Report the malaria status of this cell.
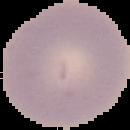

Uninfected.

Summary:
  - Image size: 130×130 pixels
  - Preparation: thin blood smear
  - Image type: cell region segmented out of the field of view; surrounding area masked to black